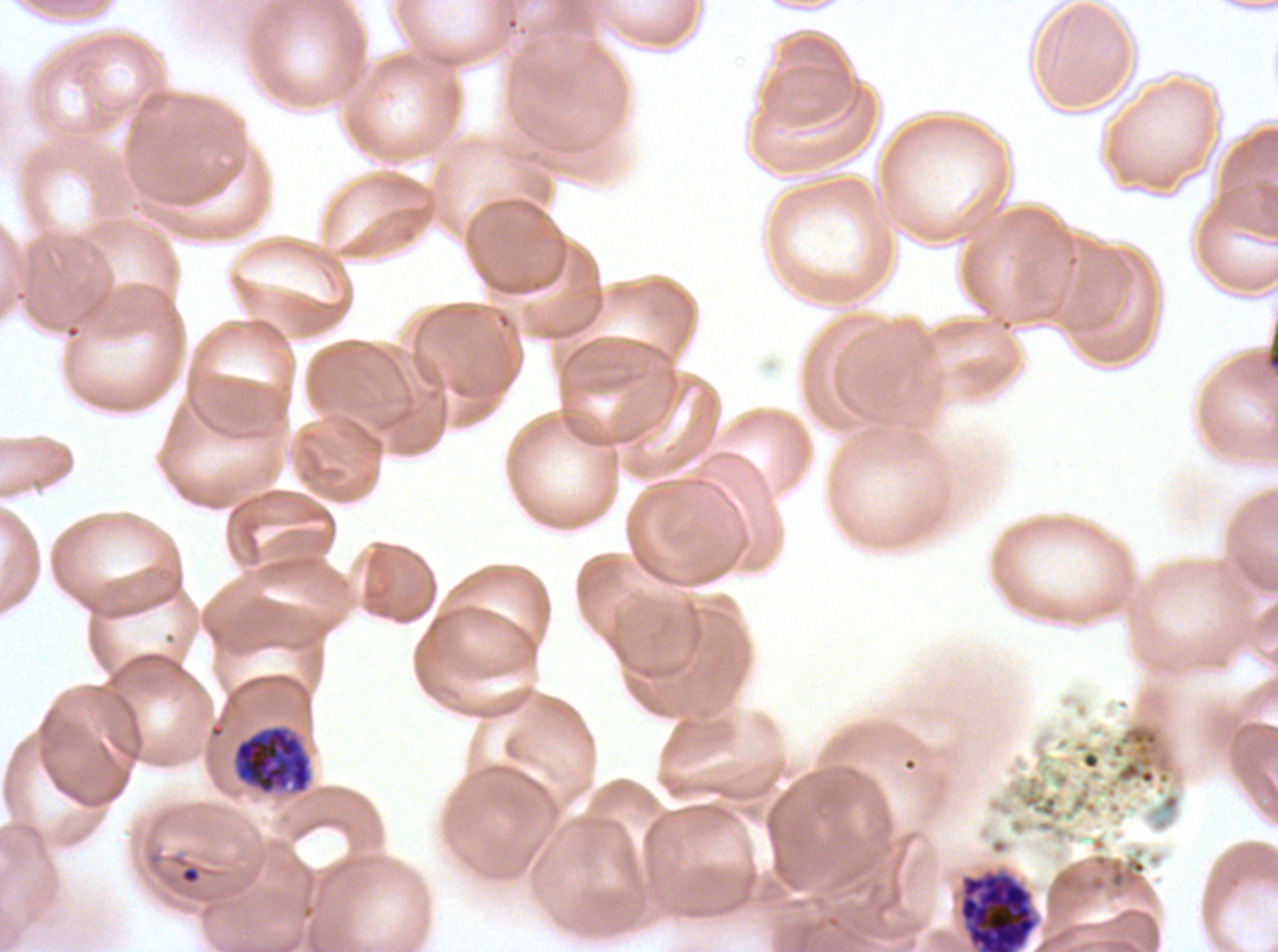
Approximate bounding boxes as {x1, y1, x2, y2} in pixels.
Summary:
  - Ring locations: {179, 865, 201, 885}
  - Late schizont locations: {959, 873, 1037, 951}
  - Early schizont locations: {233, 726, 312, 794}
  - Life-cycle stages observed: ring, early schizont, late schizont
  - Specimen: P. falciparum from a patient in The Gambia, cultured ex vivo for 24 to 48 hours
  - Stain: Giemsa
  - Image size: 1278×952 pixels
  - Preparation: thin blood smear
  - Field of view: one sub-image of a larger composite